Classify this cell by malaria status.
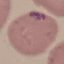

Parasitized.

image type = automatically extracted cell patch, resized to 64 × 64 pixels
capture = smartphone through the microscope eyepiece
preparation = thin blood film
stain = Giemsa